Outline each blood parasite and name the species.
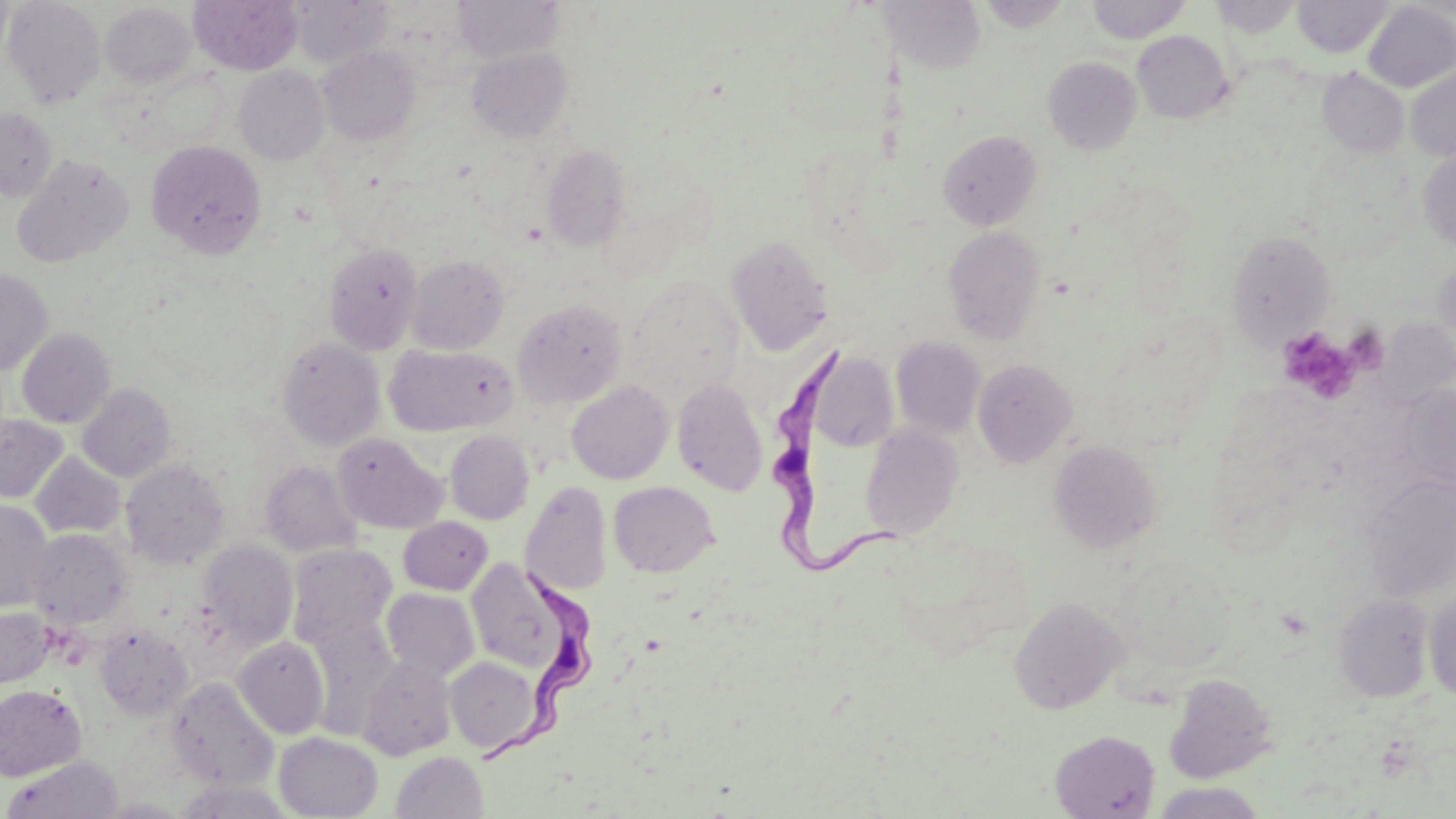

Approximate bounding boxes as (x1, y1, x2, y2) in pixels.
Trypanosoma brucei: (763, 346, 902, 576), (487, 566, 591, 767).
No Plasmodium falciparum, Plasmodium ovale, Plasmodium malariae, Plasmodium vivax, or Babesia divergens observed.

slide-level diagnosis = Trypanosoma brucei
magnification = 1000x
field of view = single
preparation = thin blood smear
modality = optical microscopy
platelet locations = approximate bounding boxes as (x1, y1, x2, y2) in pixels: (1277, 327, 1360, 401)
stain = May-Grünwald-Giemsa
uninfected red blood cell locations = approximate bounding boxes as (x1, y1, x2, y2) in pixels: (2, 0, 106, 108), (189, 0, 302, 75), (289, 0, 392, 68), (453, 0, 564, 63), (1087, 0, 1190, 44), (1208, 0, 1303, 38), (1293, 0, 1393, 58), (977, 1, 1074, 32), (889, 2, 987, 73), (1362, 2, 1456, 92), (100, 3, 198, 88), (1132, 30, 1233, 123), (317, 46, 421, 146), (466, 47, 573, 142), (1043, 57, 1142, 155), (234, 65, 330, 165), (1406, 66, 1456, 161), (1317, 68, 1409, 158), (0, 107, 57, 202), (938, 130, 1042, 231), (146, 139, 267, 258), (541, 144, 630, 251), (1417, 149, 1456, 250), (12, 153, 134, 268), (943, 226, 1046, 345), (1226, 230, 1337, 347), (726, 233, 834, 355), (324, 241, 423, 354), (406, 254, 509, 354), (1433, 261, 1456, 356), (0, 268, 53, 376), (624, 275, 744, 401), (512, 298, 628, 408), (17, 328, 116, 428), (276, 337, 385, 450), (892, 337, 986, 437), (384, 344, 515, 436), (809, 351, 899, 452), (973, 358, 1078, 467), (672, 379, 768, 496), (566, 380, 674, 484), (77, 383, 175, 482), (1398, 383, 1456, 491), (0, 416, 69, 503), (860, 425, 964, 541), (444, 430, 534, 524), (333, 432, 447, 534), (1048, 440, 1162, 553), (30, 452, 125, 538), (121, 459, 230, 569), (260, 461, 361, 557), (1360, 474, 1456, 602), (521, 481, 612, 596), (608, 481, 720, 578), (0, 499, 53, 611), (398, 517, 492, 594), (28, 529, 131, 629), (197, 540, 299, 649), (287, 544, 397, 648), (1111, 554, 1238, 673), (465, 559, 575, 675), (382, 588, 480, 681), (1334, 594, 1434, 702), (1425, 594, 1456, 701), (1009, 596, 1129, 714), (1, 605, 56, 689), (304, 615, 400, 733), (94, 626, 194, 720), (232, 637, 329, 739), (357, 655, 457, 761), (445, 656, 541, 755), (1164, 672, 1278, 783), (167, 677, 278, 790), (0, 684, 86, 781), (1050, 729, 1160, 818), (274, 732, 383, 818), (391, 751, 488, 819), (3, 756, 124, 819), (1152, 782, 1268, 818)
image size = 1456×819 pixels